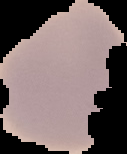
preparation = thin blood film
malaria status = uninfected
image type = cell region segmented out of the field of view; surrounding area masked to black
image size = 127×154 pixels